Identify the parasite.
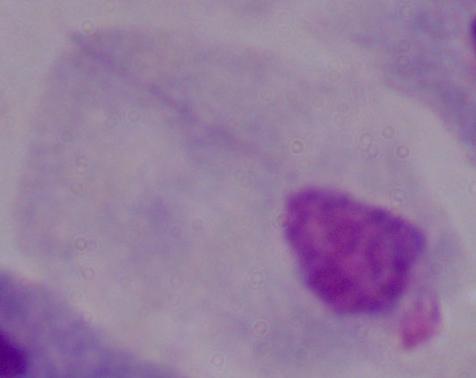

This is a trichomonad.

Photomicrograph. Captured at 1000x magnification.